Report the malaria status of this cell.
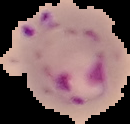
Parasitized.

Summary:
  - Image type: cell region segmented out of the field of view; surrounding area masked to black
  - Image size: 130×124 pixels
  - Preparation: thin blood film